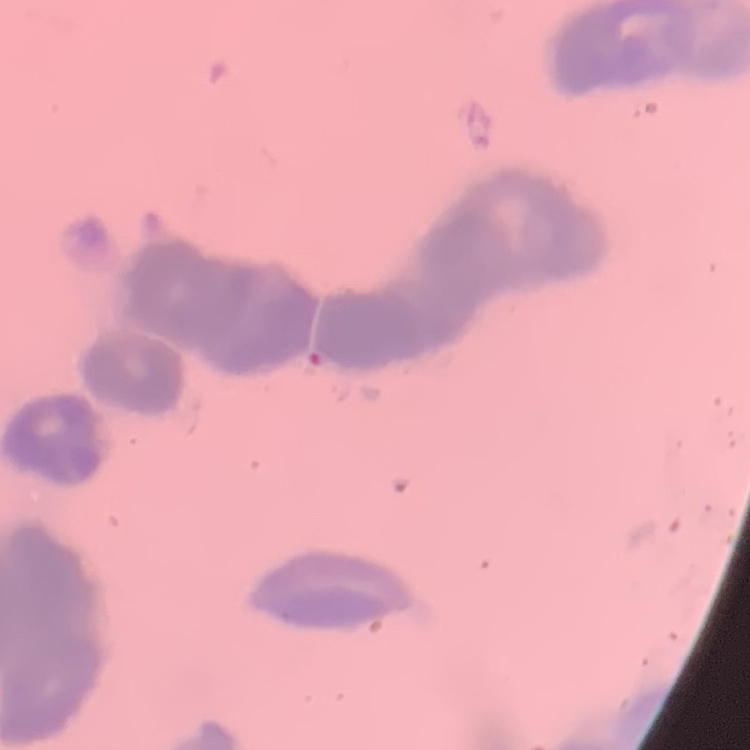
red blood cell morphology = rouleaux formation
stain = Field's or Giemsa
preparation = thin blood film
image type = square crop of a larger photomicrograph